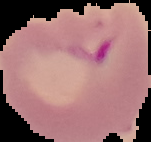

Summary:
  - Image type: segmented cell region on a black background
  - Preparation: thin blood film
  - Malaria status: parasitized
  - Image size: 151×142 pixels